Point out each Plasmodium parasite.
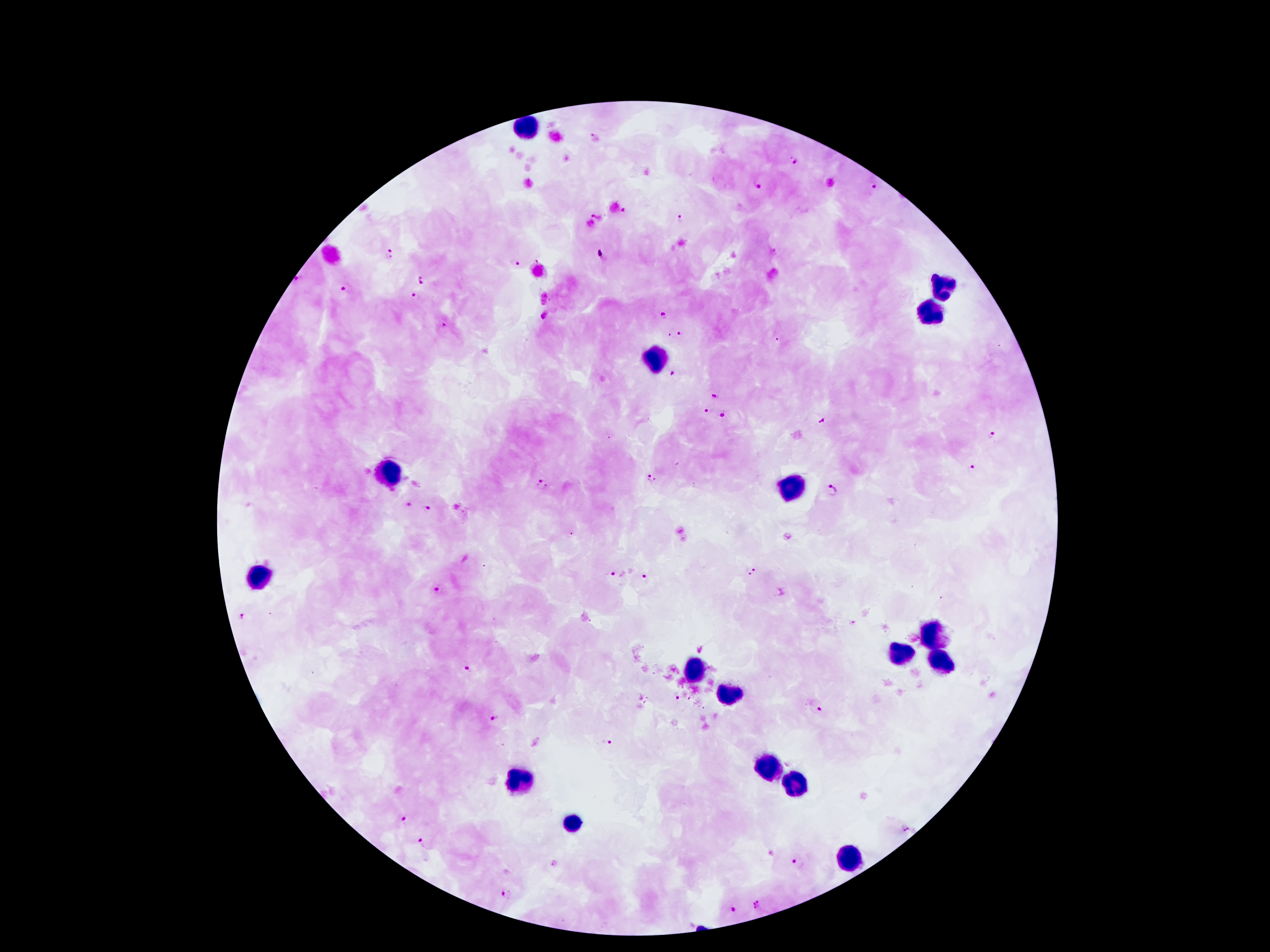
Approximate centers as (x, y) in pixels.
Plasmodium parasites: (594, 137), (796, 162), (761, 186), (873, 187), (680, 219), (390, 252), (601, 254), (514, 261), (420, 280), (345, 289), (415, 295), (663, 315), (545, 318), (444, 323), (682, 332), (672, 336), (673, 371), (717, 396), (708, 410), (723, 413), (822, 419), (994, 434), (974, 471), (653, 478), (544, 482), (832, 490), (428, 510), (751, 571), (616, 574), (644, 579), (440, 589), (243, 616), (853, 623), (468, 668), (681, 698), (816, 710), (496, 719), (610, 742), (406, 818), (905, 828), (423, 838), (799, 861), (505, 897), (759, 905), (733, 907).

Leukocyte locations: (522, 127), (947, 284), (931, 312), (657, 354), (391, 469), (790, 489), (257, 578), (936, 631), (902, 651), (697, 666), (940, 666), (728, 693), (765, 766), (518, 781), (798, 785), (573, 821), (847, 856). One field from this slide. Photographed through the microscope eyepiece with a smartphone camera. Image is 1270×952 pixels. Thick peripheral-blood smear. 100x magnification. Patient malaria status: infected with Plasmodium falciparum. Giemsa-stained preparation.